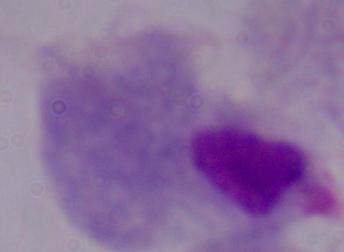

A trichomonad is shown. Captured at 1000x magnification. Photomicrograph.